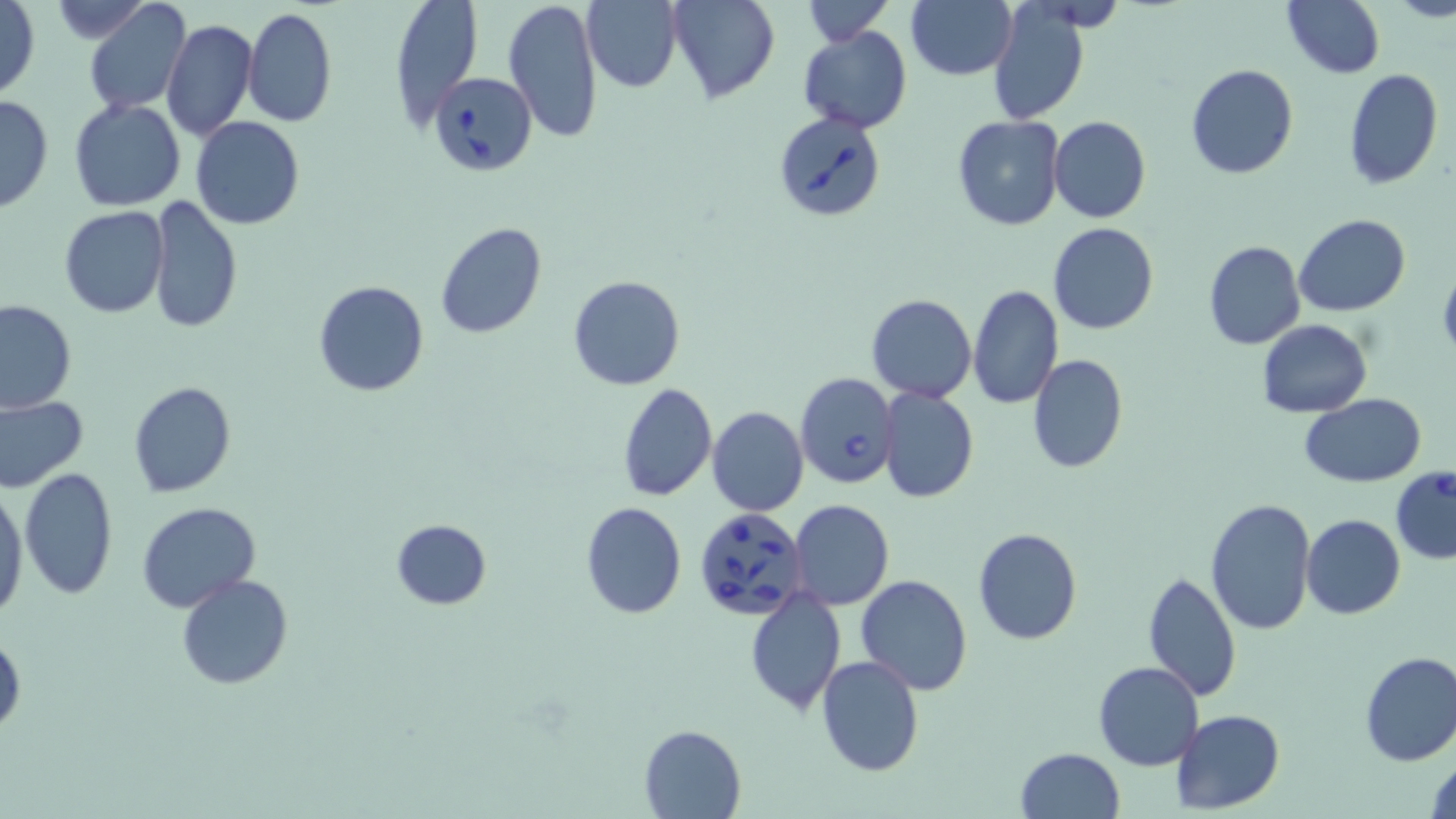

Approximate bounding boxes as named x1/y1/x2/y2 corners in pixels. Babesia divergens-infected red blood cell locations: (x1=432, y1=72, x2=537, y2=176), (x1=774, y1=112, x2=887, y2=223), (x1=795, y1=371, x2=898, y2=488), (x1=1390, y1=467, x2=1456, y2=564), (x1=694, y1=509, x2=812, y2=622). Uninfected red blood cell locations: (x1=388, y1=0, x2=483, y2=130), (x1=505, y1=0, x2=604, y2=143), (x1=582, y1=0, x2=681, y2=92), (x1=667, y1=0, x2=779, y2=104), (x1=798, y1=0, x2=894, y2=44), (x1=1282, y1=0, x2=1385, y2=78), (x1=1, y1=1, x2=41, y2=102), (x1=45, y1=1, x2=158, y2=43), (x1=84, y1=1, x2=191, y2=116), (x1=905, y1=1, x2=1016, y2=80), (x1=986, y1=4, x2=1092, y2=126), (x1=243, y1=7, x2=335, y2=126), (x1=161, y1=17, x2=256, y2=140), (x1=797, y1=26, x2=913, y2=134), (x1=1186, y1=65, x2=1298, y2=180), (x1=1344, y1=68, x2=1443, y2=189), (x1=0, y1=92, x2=53, y2=215), (x1=68, y1=98, x2=186, y2=211), (x1=952, y1=115, x2=1067, y2=233), (x1=190, y1=116, x2=305, y2=231), (x1=1048, y1=116, x2=1151, y2=224), (x1=147, y1=195, x2=241, y2=337), (x1=60, y1=206, x2=168, y2=317), (x1=1294, y1=215, x2=1411, y2=317), (x1=434, y1=222, x2=548, y2=340), (x1=1048, y1=222, x2=1159, y2=335), (x1=1202, y1=241, x2=1306, y2=351), (x1=1438, y1=265, x2=1456, y2=363), (x1=568, y1=275, x2=686, y2=391), (x1=314, y1=281, x2=429, y2=398), (x1=966, y1=283, x2=1062, y2=409), (x1=867, y1=293, x2=977, y2=403), (x1=1, y1=300, x2=76, y2=414), (x1=1258, y1=319, x2=1372, y2=418), (x1=1027, y1=355, x2=1128, y2=474), (x1=129, y1=382, x2=237, y2=498), (x1=616, y1=382, x2=717, y2=502), (x1=877, y1=385, x2=979, y2=504), (x1=1301, y1=394, x2=1425, y2=488), (x1=0, y1=396, x2=88, y2=494), (x1=707, y1=406, x2=810, y2=517), (x1=19, y1=468, x2=119, y2=598), (x1=1, y1=483, x2=29, y2=615), (x1=1205, y1=497, x2=1318, y2=635), (x1=790, y1=499, x2=894, y2=611), (x1=579, y1=501, x2=686, y2=618), (x1=137, y1=502, x2=261, y2=611), (x1=1301, y1=514, x2=1404, y2=619), (x1=390, y1=519, x2=491, y2=610), (x1=972, y1=528, x2=1082, y2=645), (x1=1143, y1=572, x2=1241, y2=701), (x1=176, y1=573, x2=295, y2=690), (x1=856, y1=575, x2=974, y2=694), (x1=744, y1=588, x2=848, y2=714), (x1=0, y1=629, x2=25, y2=738), (x1=1358, y1=651, x2=1456, y2=767), (x1=816, y1=654, x2=925, y2=776), (x1=1094, y1=660, x2=1204, y2=770), (x1=1173, y1=709, x2=1285, y2=814), (x1=639, y1=724, x2=746, y2=817), (x1=1014, y1=747, x2=1125, y2=819), (x1=1427, y1=755, x2=1455, y2=819). Slide-level diagnosis: Babesia divergens. Image is 1456×819 pixels. Single field of view. Optical microscopy. May-Grünwald-Giemsa stain. Thin blood film. 1000x magnification.